Identify the blood parasite species.
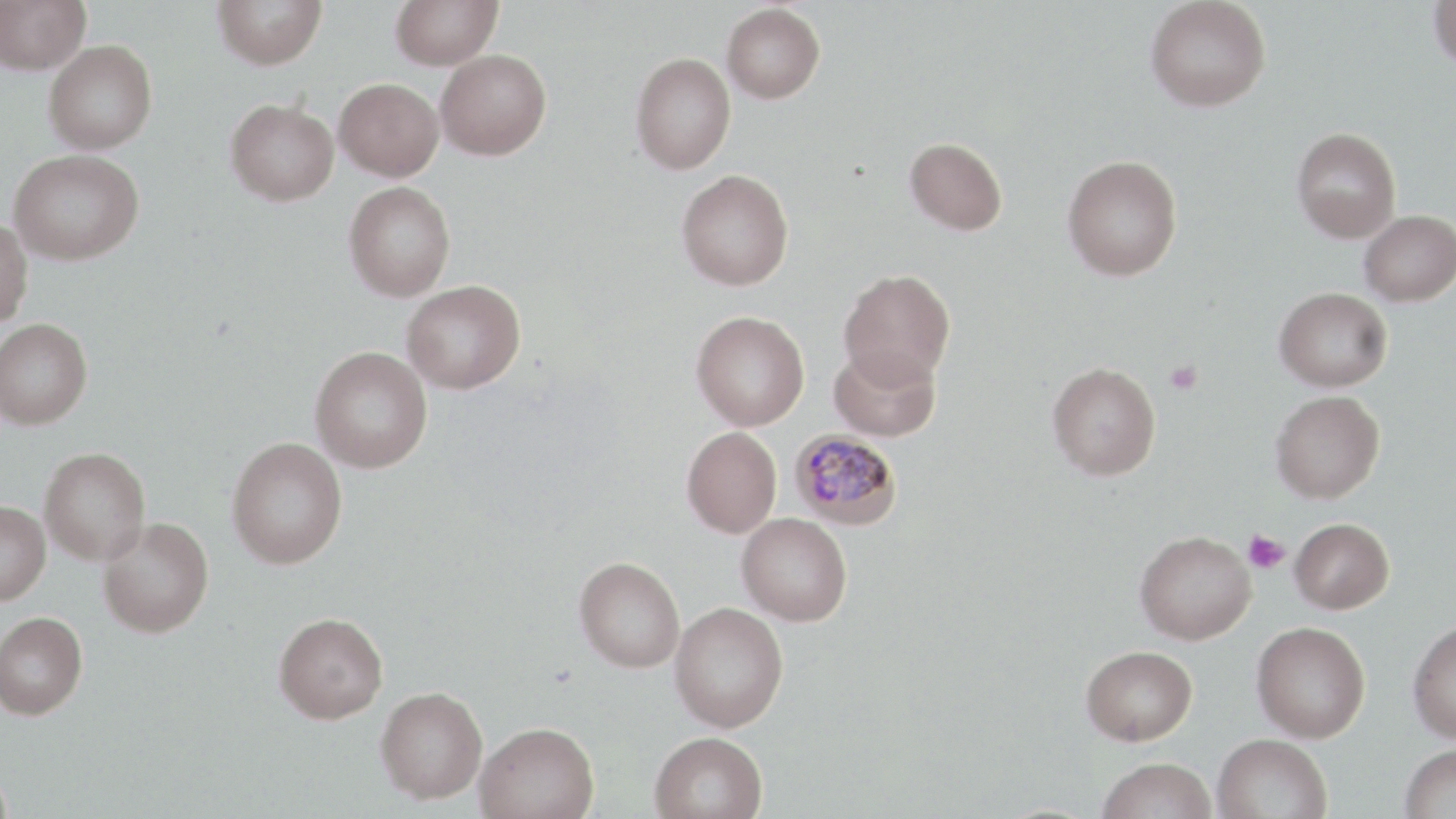
Plasmodium malariae.

preparation = thin blood film
modality = light microscopy
stain = May-Grünwald-Giemsa
Plasmodium malariae-infected red blood cell locations = approximate bounding boxes as (x1, y1, x2, y2) in pixels: (789, 428, 903, 530)
field of view = single
magnification = 1000x
uninfected red blood cell locations = approximate bounding boxes as (x1, y1, x2, y2) in pixels: (0, 0, 90, 74), (211, 0, 327, 70), (391, 0, 502, 70), (1145, 0, 1271, 112), (1428, 1, 1456, 73), (722, 3, 826, 103), (44, 39, 158, 154), (435, 49, 552, 160), (630, 52, 736, 175), (334, 77, 444, 181), (225, 98, 339, 206), (1291, 127, 1402, 242), (904, 137, 1008, 235), (8, 149, 144, 265), (1061, 154, 1182, 281), (676, 169, 794, 290), (343, 181, 456, 301), (1359, 210, 1456, 306), (0, 218, 33, 328), (838, 268, 956, 387), (401, 280, 526, 394), (1274, 287, 1392, 392), (691, 310, 809, 431), (0, 317, 92, 430), (829, 344, 941, 442), (310, 345, 433, 473), (1047, 362, 1161, 480), (1270, 390, 1385, 503), (682, 426, 782, 538), (226, 436, 347, 569), (39, 447, 151, 565), (0, 499, 50, 606), (737, 513, 852, 626), (97, 517, 214, 638), (1289, 517, 1394, 614), (1135, 531, 1256, 645), (574, 556, 685, 672), (669, 602, 788, 732), (0, 611, 88, 719), (274, 612, 388, 723), (1408, 618, 1456, 744), (1251, 621, 1371, 742), (1081, 645, 1197, 745), (375, 686, 487, 802), (475, 721, 599, 819), (649, 731, 768, 819), (1212, 733, 1333, 819), (1400, 744, 1456, 818), (1096, 758, 1217, 819), (0, 763, 13, 819)
platelet locations = approximate bounding boxes as (x1, y1, x2, y2) in pixels: (1165, 360, 1203, 395), (1242, 531, 1291, 574)
image size = 1456×819 pixels